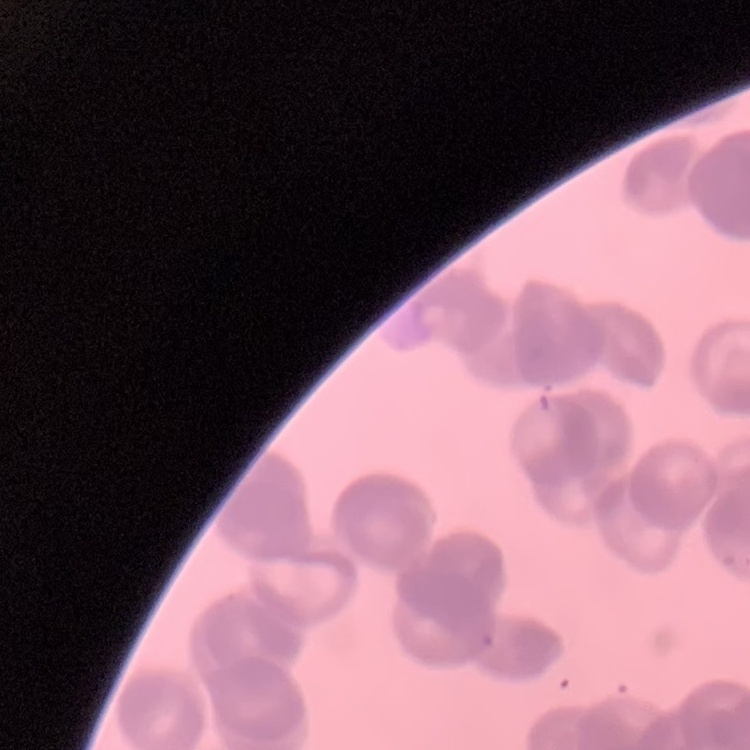
Summary:
  - Red blood cell morphology: rouleaux formation
  - Stain: Field's or Giemsa
  - Image type: one tile cut from a larger photomicrograph
  - Preparation: thin peripheral smear